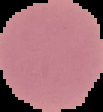

result: negative for malaria parasites
image_type: segmented cell region with the area outside set to black
image_size: 103×112 pixels
preparation: thin blood film